Name the parasite shown.
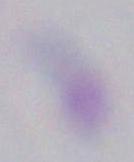

This is Toxoplasma gondii.

modality: micrograph
magnification: 1000x